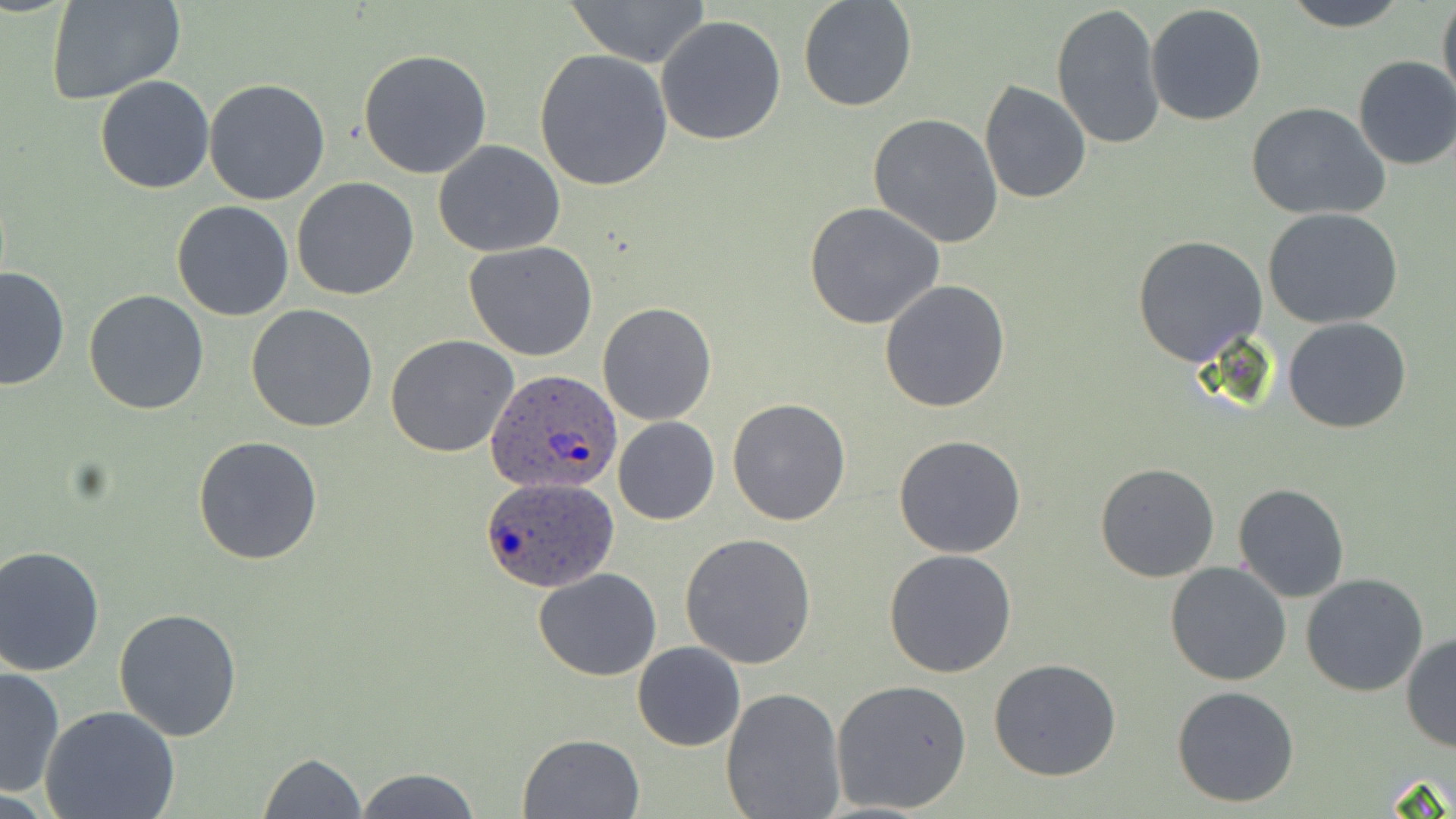

Approximate bounding boxes as named x1/y1/x2/y2 corners in pixels. Plasmodium ovale-infected red blood cell locations: (x1=487, y1=368, x2=625, y2=498), (x1=481, y1=475, x2=618, y2=594). Uninfected red blood cell locations: (x1=45, y1=0, x2=184, y2=106), (x1=560, y1=0, x2=713, y2=67), (x1=797, y1=0, x2=920, y2=113), (x1=1282, y1=0, x2=1410, y2=31), (x1=1437, y1=0, x2=1456, y2=109), (x1=1051, y1=4, x2=1166, y2=151), (x1=1145, y1=4, x2=1268, y2=127), (x1=655, y1=15, x2=787, y2=146), (x1=358, y1=48, x2=492, y2=179), (x1=534, y1=49, x2=674, y2=192), (x1=1352, y1=56, x2=1456, y2=171), (x1=94, y1=74, x2=215, y2=193), (x1=204, y1=79, x2=331, y2=204), (x1=979, y1=81, x2=1091, y2=204), (x1=1246, y1=102, x2=1392, y2=221), (x1=868, y1=113, x2=1003, y2=248), (x1=433, y1=140, x2=566, y2=257), (x1=291, y1=177, x2=421, y2=301), (x1=170, y1=200, x2=294, y2=321), (x1=805, y1=202, x2=945, y2=328), (x1=1263, y1=207, x2=1403, y2=329), (x1=1133, y1=233, x2=1268, y2=365), (x1=464, y1=241, x2=598, y2=360), (x1=0, y1=266, x2=71, y2=392), (x1=878, y1=279, x2=1010, y2=413), (x1=83, y1=290, x2=210, y2=415), (x1=598, y1=302, x2=717, y2=426), (x1=246, y1=304, x2=379, y2=432), (x1=1283, y1=316, x2=1411, y2=433), (x1=386, y1=335, x2=518, y2=458), (x1=727, y1=398, x2=851, y2=525), (x1=614, y1=416, x2=720, y2=525), (x1=895, y1=435, x2=1026, y2=557), (x1=192, y1=436, x2=325, y2=565), (x1=1095, y1=463, x2=1220, y2=583), (x1=1232, y1=483, x2=1350, y2=602), (x1=682, y1=532, x2=818, y2=669), (x1=0, y1=545, x2=106, y2=677), (x1=883, y1=549, x2=1016, y2=678), (x1=1165, y1=561, x2=1292, y2=686), (x1=533, y1=567, x2=661, y2=681), (x1=1301, y1=573, x2=1430, y2=696), (x1=112, y1=606, x2=243, y2=741), (x1=1401, y1=633, x2=1456, y2=751), (x1=632, y1=641, x2=745, y2=751), (x1=988, y1=658, x2=1122, y2=782), (x1=1, y1=665, x2=65, y2=796), (x1=831, y1=678, x2=972, y2=814), (x1=1170, y1=685, x2=1301, y2=808), (x1=720, y1=688, x2=846, y2=819), (x1=40, y1=706, x2=182, y2=819), (x1=516, y1=733, x2=644, y2=818), (x1=258, y1=752, x2=366, y2=819), (x1=352, y1=766, x2=482, y2=819). Slide-level diagnosis: Plasmodium ovale. One field of a larger specimen. Light microscopy. May-Grünwald-Giemsa-stained preparation. Captured at 1000x magnification. Thin blood smear. Image is 1456×819 pixels.